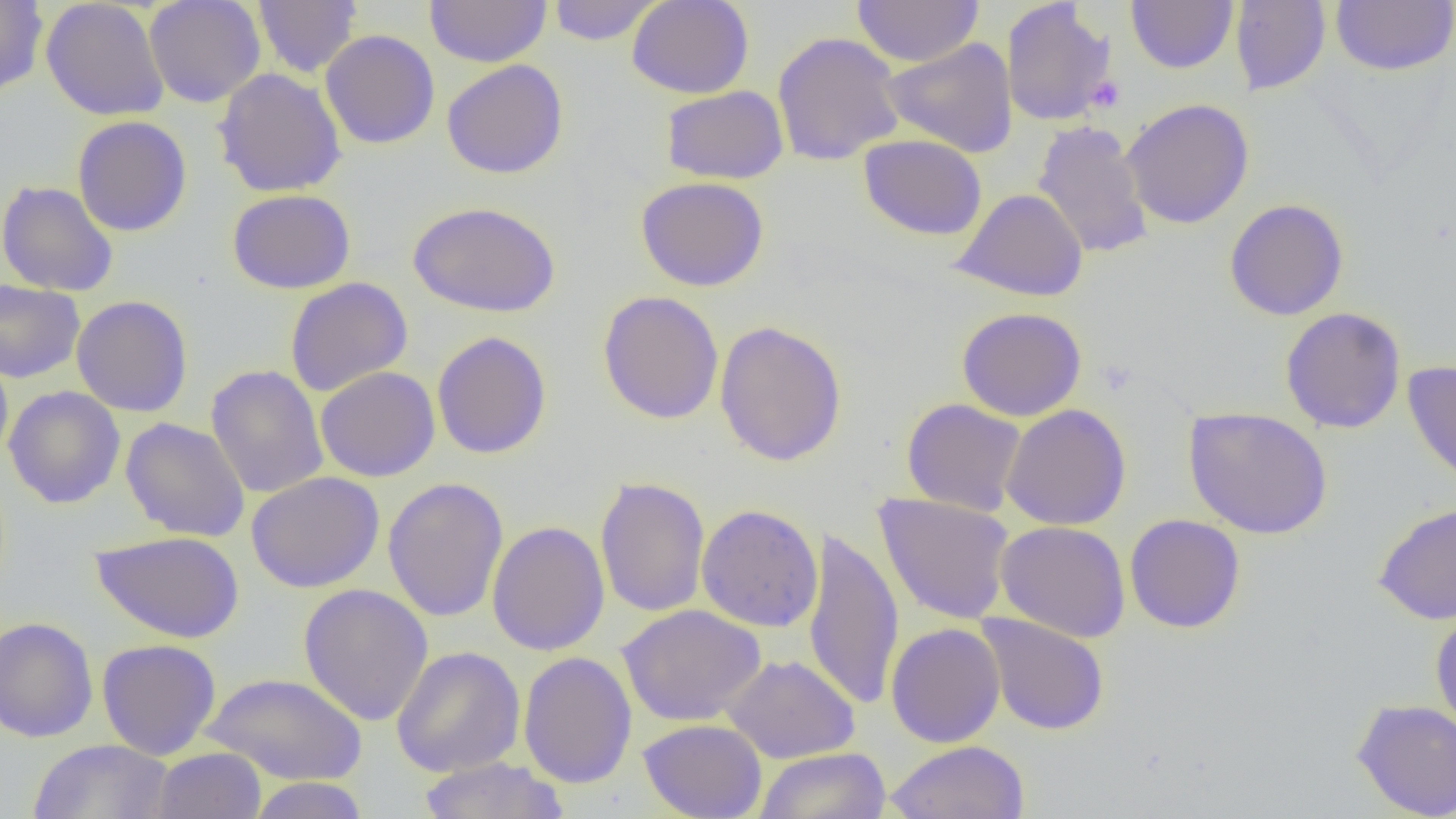
Approximate bounding boxes as named x1/y1/x2/y2 corners in pixels. Uninfected red blood cell locations: (x1=0, y1=0, x2=48, y2=98), (x1=143, y1=0, x2=266, y2=107), (x1=253, y1=0, x2=362, y2=77), (x1=425, y1=0, x2=552, y2=67), (x1=626, y1=0, x2=754, y2=99), (x1=851, y1=0, x2=984, y2=67), (x1=1126, y1=0, x2=1238, y2=73), (x1=1330, y1=0, x2=1456, y2=75), (x1=41, y1=1, x2=170, y2=121), (x1=547, y1=1, x2=663, y2=45), (x1=1230, y1=1, x2=1331, y2=96), (x1=1001, y1=2, x2=1117, y2=126), (x1=320, y1=29, x2=440, y2=149), (x1=772, y1=31, x2=906, y2=167), (x1=882, y1=37, x2=1018, y2=157), (x1=442, y1=59, x2=569, y2=179), (x1=213, y1=67, x2=347, y2=197), (x1=660, y1=85, x2=789, y2=184), (x1=1120, y1=98, x2=1255, y2=229), (x1=72, y1=116, x2=192, y2=236), (x1=1032, y1=120, x2=1154, y2=259), (x1=859, y1=134, x2=988, y2=240), (x1=635, y1=176, x2=769, y2=292), (x1=0, y1=180, x2=119, y2=297), (x1=952, y1=188, x2=1089, y2=302), (x1=227, y1=189, x2=356, y2=294), (x1=1224, y1=199, x2=1349, y2=321), (x1=408, y1=201, x2=561, y2=318), (x1=284, y1=277, x2=413, y2=397), (x1=0, y1=279, x2=85, y2=383), (x1=597, y1=290, x2=724, y2=425), (x1=71, y1=295, x2=193, y2=417), (x1=956, y1=306, x2=1087, y2=422), (x1=1280, y1=307, x2=1407, y2=433), (x1=714, y1=319, x2=848, y2=467), (x1=431, y1=331, x2=552, y2=459), (x1=0, y1=351, x2=13, y2=466), (x1=1402, y1=360, x2=1456, y2=490), (x1=205, y1=364, x2=328, y2=499), (x1=315, y1=366, x2=441, y2=482), (x1=4, y1=386, x2=125, y2=508), (x1=901, y1=398, x2=1027, y2=516), (x1=1001, y1=403, x2=1131, y2=530), (x1=1183, y1=406, x2=1333, y2=539), (x1=120, y1=417, x2=250, y2=541), (x1=246, y1=471, x2=384, y2=593), (x1=594, y1=476, x2=711, y2=617), (x1=382, y1=477, x2=509, y2=622), (x1=874, y1=492, x2=1015, y2=625), (x1=1373, y1=502, x2=1456, y2=625), (x1=696, y1=504, x2=824, y2=632), (x1=1124, y1=514, x2=1246, y2=633), (x1=486, y1=520, x2=610, y2=656), (x1=994, y1=521, x2=1131, y2=642), (x1=803, y1=525, x2=904, y2=711), (x1=91, y1=530, x2=244, y2=643), (x1=298, y1=583, x2=434, y2=726), (x1=617, y1=604, x2=766, y2=725), (x1=1430, y1=608, x2=1456, y2=734), (x1=975, y1=613, x2=1110, y2=736), (x1=0, y1=616, x2=99, y2=743), (x1=885, y1=622, x2=1006, y2=747), (x1=96, y1=638, x2=221, y2=760), (x1=391, y1=646, x2=526, y2=777), (x1=518, y1=651, x2=637, y2=789), (x1=721, y1=654, x2=861, y2=763), (x1=202, y1=672, x2=368, y2=786), (x1=1351, y1=698, x2=1456, y2=818), (x1=638, y1=718, x2=767, y2=819), (x1=27, y1=738, x2=176, y2=818), (x1=886, y1=740, x2=1030, y2=819), (x1=151, y1=747, x2=266, y2=819), (x1=755, y1=747, x2=891, y2=819), (x1=418, y1=757, x2=569, y2=818), (x1=246, y1=777, x2=369, y2=818). Platelet locations: (x1=1085, y1=75, x2=1127, y2=114). Slide-level diagnosis: negative for blood parasites. Image is 1456×819 pixels. Thin blood smear. Single field of view. Optical microscopy. Captured at 1000x magnification.